State which parasite is depicted.
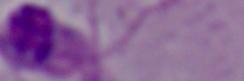
Leishmania.

Micrograph. Captured at 1000x magnification.